Name the parasite shown.
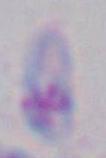

Toxoplasma gondii.

{
  "modality": "photomicrograph",
  "magnification": "1000x"
}